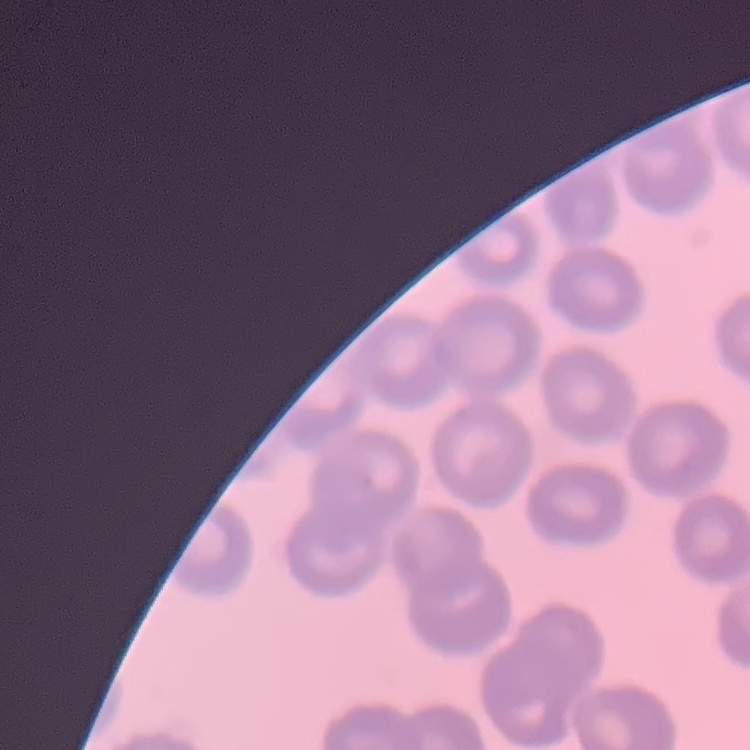
Summary:
  - Erythrocyte morphology: no rouleaux formation
  - Stain: Field's or Giemsa
  - Preparation: thin blood smear
  - Image type: one tile cut from a larger photomicrograph